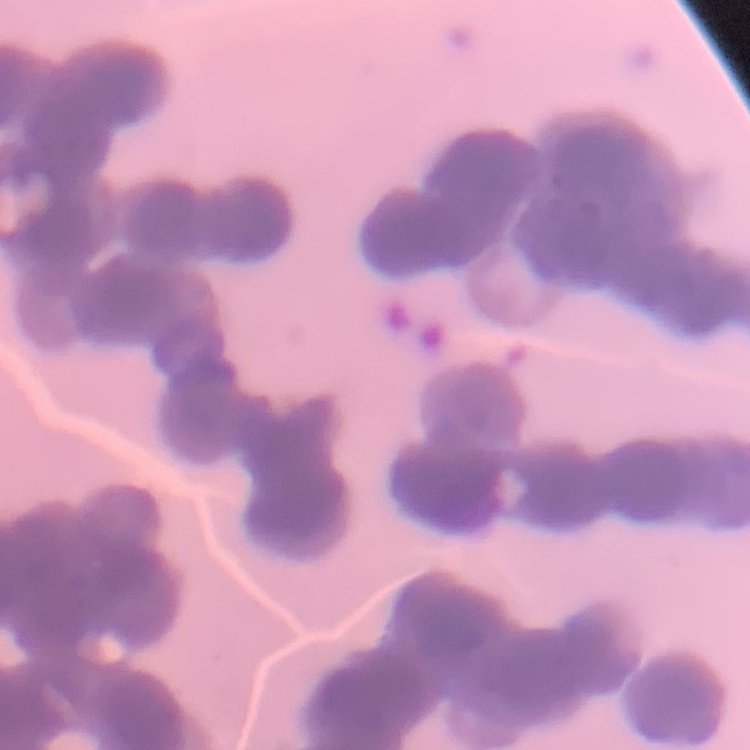

The red blood cells exhibit rouleaux formation. Stained with either Field's or Giemsa. Thin blood smear. One tile cut from a larger photomicrograph.